Locate leukocytes (white blood cells).
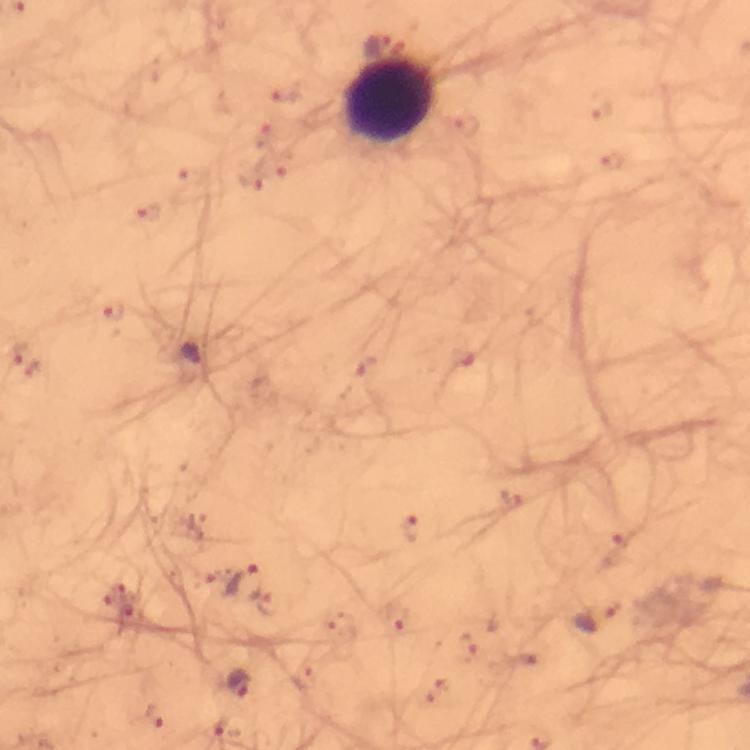
Approximate centers as {x, y} in pixels.
Leukocytes: {392, 104}.

{
  "preparation": "thick smear",
  "immersion_oil": "used",
  "capture": "smartphone camera through the microscope",
  "stain": "Giemsa",
  "plasmodium_parasite_locations": "approximate centers as {x, y} in pixels: {19, 352}, {192, 352}, {367, 364}, {34, 368}, {412, 529}, {128, 581}, {243, 582}, {132, 617}, {396, 617}, {597, 617}, {237, 683}, {153, 716}",
  "magnification": "100x",
  "image_size": "750×750 pixels",
  "cropped_from": "a single field of view",
  "context": "from a diagnostic examination for malaria"
}